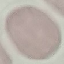
Result: negative for malaria parasites. Automatically extracted cell patch, resized to 64 × 64 pixels. Photographed with a smartphone camera at the microscope eyepiece. Thin blood film. Giemsa-stained preparation.